Classify this cell by malaria status.
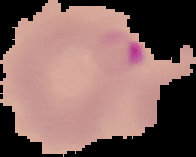
Parasitized.

Summary:
  - Image type: segmented cell region on a black background
  - Preparation: thin blood smear
  - Image size: 196×157 pixels